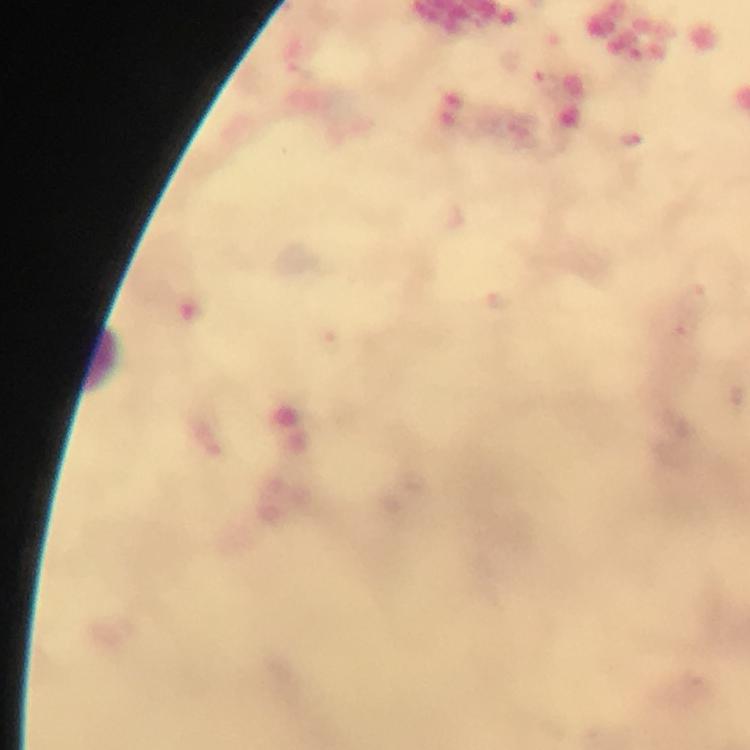
Approximate object centers, in pixels from the top-left corner.
Summary:
  - Leukocyte locations: (x=98, y=360)
  - Malaria parasites: none seen
  - Image size: 750×750 pixels
  - Magnification: 100x
  - Capture: smartphone mounted on the microscope
  - Preparation: thick blood smear
  - Cropped from: one field of view
  - Stain: Giemsa
  - Context: from a diagnostic examination for malaria
  - Immersion oil: applied